Name the blood parasite species.
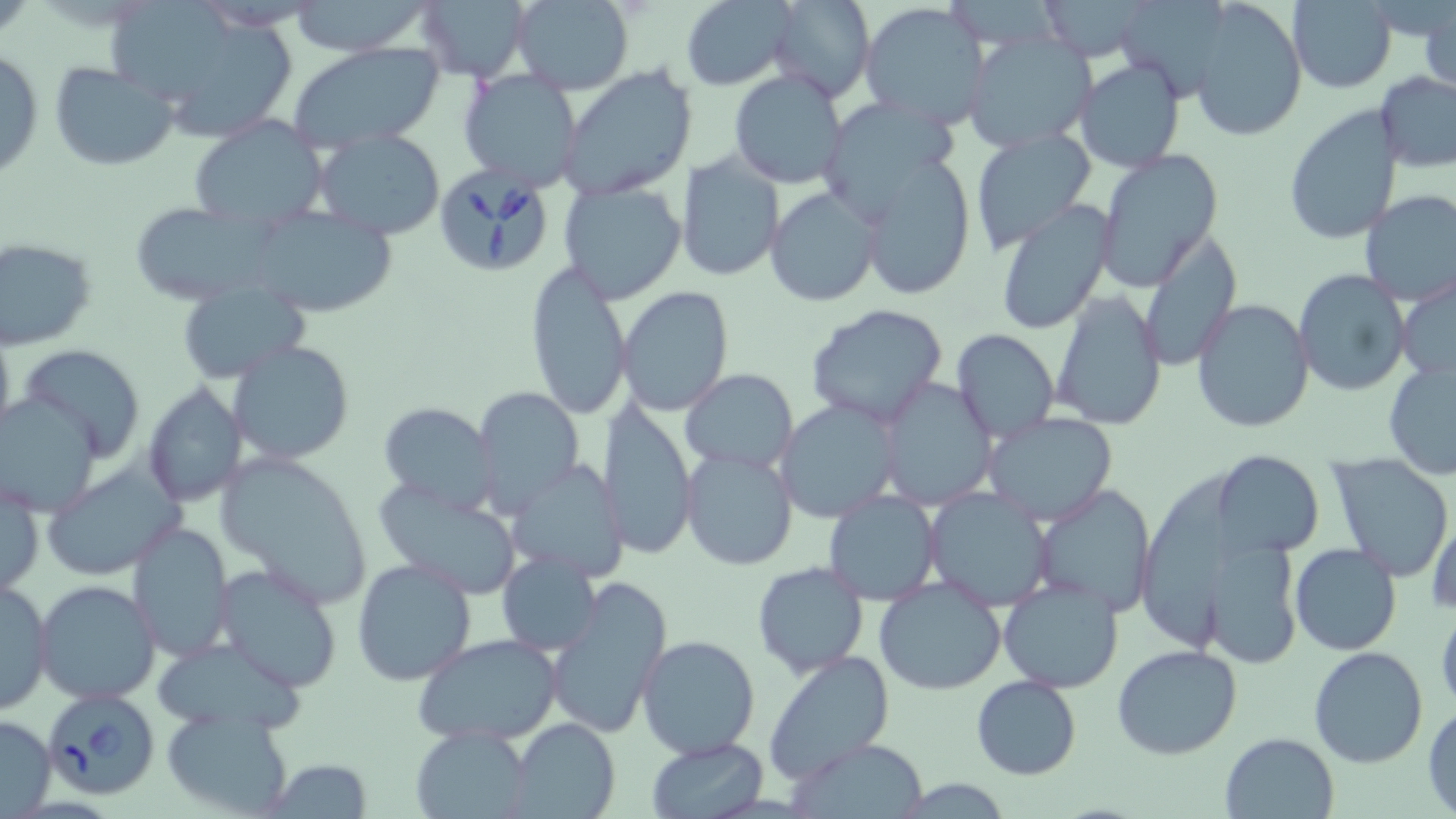
Babesia divergens.

Approximate bounding boxes as named x1/y1/x2/y2 corners in pixels. Babesia divergens-infected red blood cell locations: (x1=432, y1=162, x2=556, y2=276), (x1=41, y1=689, x2=162, y2=800). Uninfected red blood cell locations: (x1=415, y1=0, x2=532, y2=83), (x1=510, y1=0, x2=634, y2=95), (x1=764, y1=0, x2=874, y2=103), (x1=1034, y1=0, x2=1160, y2=62), (x1=1189, y1=0, x2=1307, y2=141), (x1=1286, y1=0, x2=1398, y2=93), (x1=110, y1=1, x2=235, y2=100), (x1=680, y1=1, x2=794, y2=89), (x1=285, y1=2, x2=434, y2=56), (x1=860, y1=2, x2=990, y2=128), (x1=1122, y1=4, x2=1234, y2=98), (x1=1420, y1=6, x2=1455, y2=99), (x1=169, y1=20, x2=299, y2=147), (x1=963, y1=31, x2=1096, y2=155), (x1=287, y1=40, x2=448, y2=151), (x1=0, y1=47, x2=45, y2=183), (x1=1075, y1=58, x2=1186, y2=174), (x1=48, y1=62, x2=179, y2=172), (x1=559, y1=64, x2=699, y2=199), (x1=458, y1=68, x2=583, y2=191), (x1=728, y1=70, x2=849, y2=190), (x1=1376, y1=73, x2=1456, y2=172), (x1=828, y1=100, x2=962, y2=209), (x1=1282, y1=104, x2=1404, y2=246), (x1=187, y1=115, x2=331, y2=232), (x1=968, y1=126, x2=1096, y2=253), (x1=314, y1=129, x2=448, y2=240), (x1=1095, y1=151, x2=1224, y2=292), (x1=676, y1=152, x2=784, y2=283), (x1=858, y1=156, x2=975, y2=301), (x1=558, y1=180, x2=686, y2=304), (x1=765, y1=184, x2=884, y2=308), (x1=1358, y1=189, x2=1456, y2=306), (x1=994, y1=203, x2=1115, y2=335), (x1=127, y1=204, x2=269, y2=300), (x1=247, y1=208, x2=395, y2=316), (x1=1136, y1=231, x2=1241, y2=369), (x1=0, y1=239, x2=97, y2=349), (x1=524, y1=262, x2=632, y2=420), (x1=1293, y1=269, x2=1411, y2=396), (x1=1396, y1=277, x2=1456, y2=387), (x1=177, y1=282, x2=308, y2=383), (x1=617, y1=286, x2=734, y2=416), (x1=1048, y1=290, x2=1168, y2=430), (x1=1191, y1=297, x2=1315, y2=435), (x1=803, y1=304, x2=953, y2=430), (x1=952, y1=329, x2=1059, y2=444), (x1=229, y1=341, x2=354, y2=465), (x1=18, y1=344, x2=145, y2=460), (x1=1382, y1=358, x2=1456, y2=482), (x1=682, y1=368, x2=798, y2=472), (x1=879, y1=380, x2=997, y2=510), (x1=142, y1=383, x2=249, y2=508), (x1=474, y1=388, x2=585, y2=517), (x1=0, y1=393, x2=104, y2=516), (x1=776, y1=398, x2=901, y2=523), (x1=595, y1=400, x2=698, y2=560), (x1=379, y1=401, x2=498, y2=510), (x1=984, y1=413, x2=1119, y2=525), (x1=681, y1=447, x2=797, y2=569), (x1=212, y1=449, x2=372, y2=607), (x1=1211, y1=450, x2=1323, y2=558), (x1=1328, y1=455, x2=1455, y2=580), (x1=506, y1=460, x2=632, y2=584), (x1=44, y1=462, x2=183, y2=581), (x1=1137, y1=469, x2=1243, y2=654), (x1=1, y1=475, x2=43, y2=600), (x1=372, y1=481, x2=526, y2=597), (x1=1035, y1=485, x2=1154, y2=617), (x1=927, y1=486, x2=1053, y2=607), (x1=824, y1=490, x2=940, y2=605), (x1=1427, y1=508, x2=1456, y2=618), (x1=127, y1=521, x2=235, y2=664), (x1=1195, y1=539, x2=1304, y2=671), (x1=1289, y1=543, x2=1400, y2=656), (x1=499, y1=551, x2=600, y2=655), (x1=352, y1=556, x2=476, y2=685), (x1=752, y1=561, x2=868, y2=678), (x1=212, y1=563, x2=342, y2=692), (x1=874, y1=575, x2=1006, y2=696), (x1=998, y1=576, x2=1126, y2=694), (x1=546, y1=577, x2=671, y2=740), (x1=1, y1=578, x2=53, y2=715), (x1=33, y1=579, x2=162, y2=704), (x1=1436, y1=607, x2=1456, y2=713), (x1=156, y1=629, x2=307, y2=734), (x1=637, y1=633, x2=762, y2=758), (x1=416, y1=636, x2=563, y2=747), (x1=1112, y1=644, x2=1243, y2=760), (x1=1308, y1=645, x2=1431, y2=768), (x1=762, y1=651, x2=896, y2=785), (x1=972, y1=675, x2=1082, y2=779), (x1=1425, y1=704, x2=1456, y2=815), (x1=159, y1=706, x2=295, y2=817), (x1=0, y1=712, x2=55, y2=816), (x1=511, y1=717, x2=621, y2=819), (x1=413, y1=728, x2=533, y2=818), (x1=1220, y1=731, x2=1340, y2=818), (x1=646, y1=736, x2=768, y2=816), (x1=793, y1=740, x2=930, y2=817), (x1=263, y1=760, x2=374, y2=817). May-Grünwald-Giemsa stain. Thin blood smear. Image is 1456×819 pixels. Light microscopy. One field of a larger specimen. Captured at 1000x magnification.